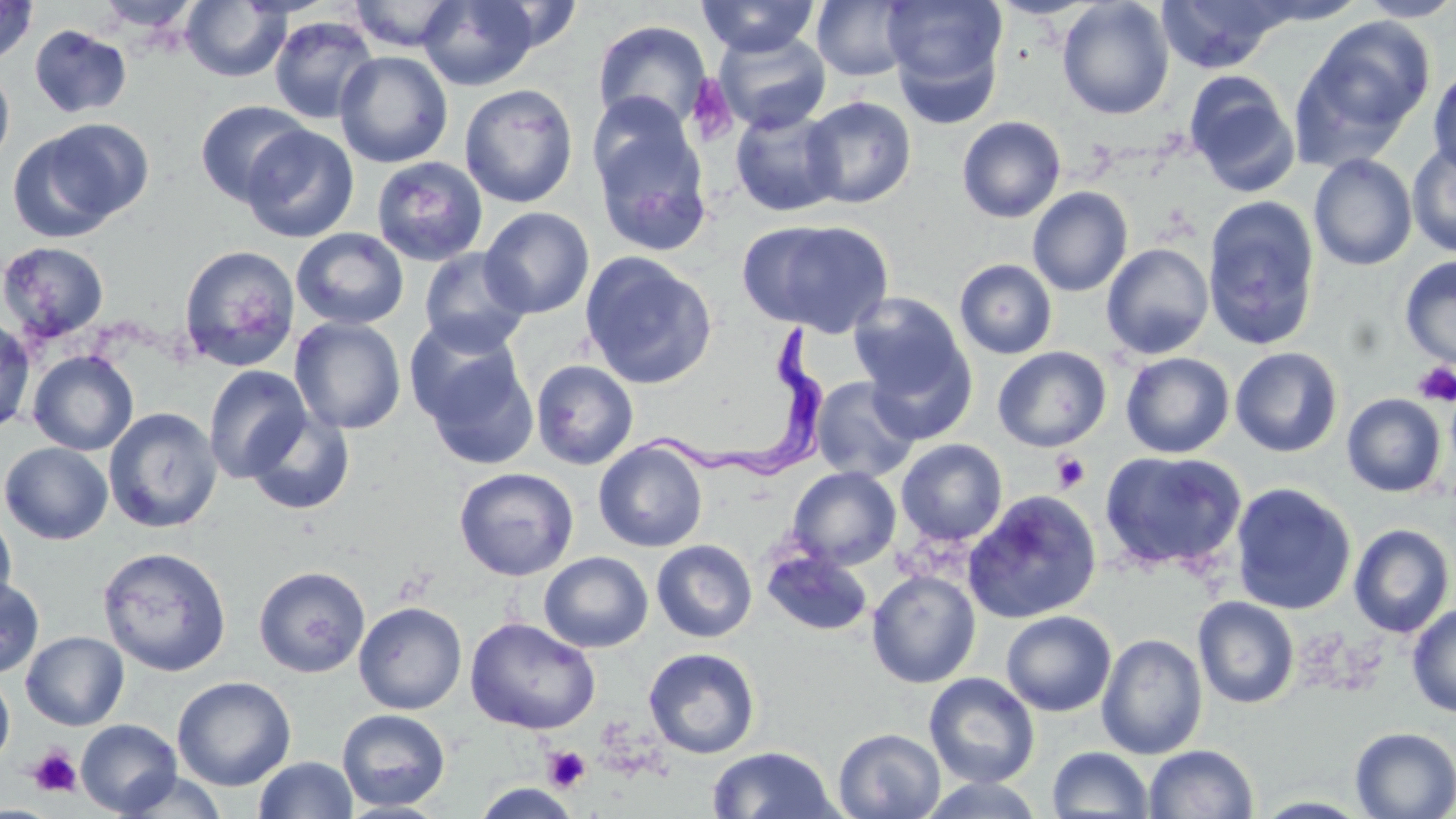
Summary:
  - Coordinate format: approximate bounding boxes as (x1,y1)-(x2,y2) corner pairs in pixels
  - Platelet locations: (685,75)-(737,144), (1413,362)-(1456,406), (1052,452)-(1090,494), (27,746)-(82,798), (542,746)-(591,792)
  - Uninfected red blood cell locations: (0,0)-(37,65), (95,0)-(201,32), (345,0)-(467,53), (696,0)-(820,57), (988,0)-(1101,19), (1057,0)-(1174,120), (1156,0)-(1291,73), (1356,0)-(1456,22), (181,1)-(289,82), (418,1)-(543,90), (812,1)-(913,81), (883,1)-(1008,110), (269,15)-(379,125), (1304,16)-(1435,145), (592,20)-(712,133), (29,24)-(131,119), (713,29)-(831,135), (335,51)-(453,168), (0,63)-(15,170), (1428,65)-(1456,176), (1185,72)-(1300,197), (459,84)-(579,207), (801,96)-(916,208), (194,100)-(311,205), (588,103)-(713,257), (730,107)-(844,217), (957,116)-(1066,223), (12,120)-(151,238), (240,124)-(359,243), (1407,142)-(1456,258), (1309,154)-(1417,271), (370,157)-(488,267), (1027,187)-(1133,297), (1203,196)-(1321,351), (480,206)-(594,319), (741,219)-(895,337), (292,228)-(409,330), (0,241)-(109,343), (1101,242)-(1214,359), (177,244)-(300,371), (417,247)-(533,357), (580,252)-(718,389), (1399,256)-(1456,369), (955,259)-(1058,359), (849,293)-(970,402), (290,316)-(407,435), (0,317)-(35,434), (412,334)-(539,470), (864,342)-(978,444), (993,346)-(1111,451), (1229,347)-(1343,457), (28,350)-(139,456), (1120,352)-(1235,458), (531,359)-(639,470), (203,365)-(311,483), (810,376)-(920,482), (1342,393)-(1447,497), (104,406)-(223,534), (244,409)-(355,516), (896,438)-(1008,546), (593,440)-(708,552), (1,442)-(114,545), (1098,450)-(1247,575), (787,466)-(901,570), (454,467)-(578,581), (1229,482)-(1357,615), (963,491)-(1102,624), (0,508)-(17,614), (1349,523)-(1455,638), (651,539)-(758,642), (97,546)-(231,676), (762,548)-(873,635), (539,551)-(653,653), (253,564)-(370,678), (867,569)-(981,688), (0,577)-(44,678), (1192,596)-(1300,709), (354,601)-(467,714), (1407,603)-(1456,719), (1001,610)-(1116,716), (465,617)-(600,735), (21,631)-(129,731), (1096,632)-(1208,760), (643,647)-(761,759), (0,670)-(15,768), (924,672)-(1040,788), (172,676)-(296,790), (337,709)-(451,811), (75,719)-(182,816), (1350,727)-(1456,818), (834,728)-(945,818), (1144,744)-(1259,818), (707,745)-(841,818), (1047,747)-(1154,818), (253,756)-(358,819), (114,770)-(230,818), (917,777)-(1047,818), (472,783)-(582,818)
  - Trypanosoma brucei locations: (641,320)-(831,475)
  - Slide-level diagnosis: Trypanosoma brucei
  - Field of view: single
  - Preparation: thin blood film
  - Image size: 1456×819 pixels
  - Stain: May-Grünwald-Giemsa
  - Modality: optical microscopy
  - Magnification: 1000x